Report the malaria status of this cell.
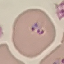
Parasitized.

Giemsa-stained preparation. Thin blood film. Automatically extracted cell patch, resized to 64 × 64 pixels. Acquired by smartphone through the microscope eyepiece.